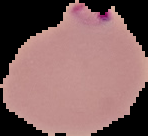
Summary:
  - Image type: segmented cell region on a black background
  - Preparation: thin blood film
  - Image size: 148×136 pixels
  - Result: malaria parasites identified